Locate and identify every blood parasite.
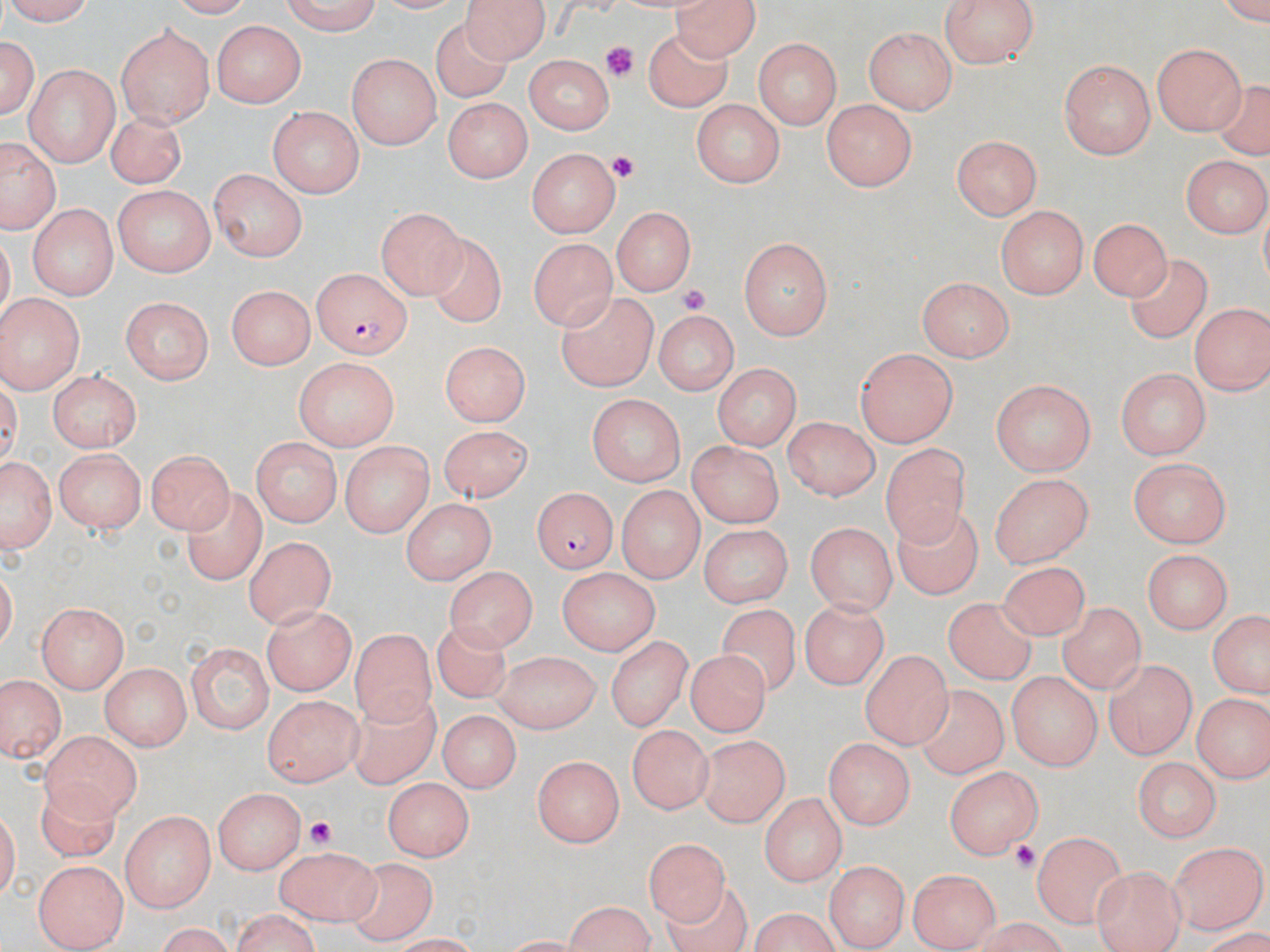
Approximate bounding boxes as (x1, y1, x2, y2) in pixels.
Plasmodium falciparum-infected red blood cells: (312, 266, 411, 358), (530, 488, 617, 574).
No Plasmodium ovale, Plasmodium malariae, Plasmodium vivax, Babesia divergens, or Trypanosoma brucei observed.

Uninfected red blood cell locations: (1, 0, 103, 26), (273, 0, 380, 35), (462, 0, 552, 62), (670, 0, 763, 57), (941, 1, 1041, 68), (429, 19, 511, 102), (209, 20, 310, 106), (114, 24, 213, 126), (865, 27, 956, 113), (645, 30, 734, 113), (0, 31, 38, 119), (751, 37, 844, 128), (1152, 39, 1247, 135), (348, 54, 439, 151), (524, 56, 615, 133), (1060, 60, 1157, 159), (23, 63, 118, 165), (1210, 81, 1270, 154), (445, 96, 529, 184), (689, 99, 787, 186), (821, 99, 919, 192), (268, 105, 366, 198), (101, 112, 188, 186), (951, 134, 1044, 223), (0, 135, 60, 236), (527, 146, 622, 237), (1180, 154, 1269, 238), (209, 169, 305, 262), (111, 186, 213, 276), (27, 202, 115, 301), (613, 204, 696, 293), (996, 205, 1090, 297), (376, 207, 463, 297), (1091, 214, 1172, 299), (430, 234, 510, 331), (526, 236, 620, 328), (739, 236, 834, 342), (1126, 257, 1213, 343), (918, 276, 1014, 360), (227, 284, 316, 370), (557, 292, 656, 390), (0, 294, 84, 395), (120, 297, 212, 385), (1188, 301, 1270, 394), (654, 310, 739, 394), (440, 342, 530, 429), (856, 349, 958, 447), (294, 356, 401, 452), (713, 364, 798, 452), (47, 367, 145, 452), (1114, 368, 1212, 457), (992, 381, 1096, 476), (585, 393, 686, 487), (779, 417, 883, 498), (435, 425, 535, 500), (250, 437, 338, 526), (341, 441, 431, 539), (687, 442, 782, 526), (880, 442, 970, 546), (54, 447, 144, 533), (147, 448, 233, 533), (0, 451, 55, 557), (1129, 454, 1229, 546), (990, 472, 1091, 569), (616, 484, 703, 583), (183, 485, 264, 590), (398, 498, 498, 582), (891, 508, 984, 597), (806, 519, 897, 612), (696, 523, 791, 607), (243, 536, 335, 628), (1142, 551, 1230, 635), (995, 562, 1097, 644), (444, 565, 536, 657), (555, 569, 657, 654), (946, 594, 1042, 683), (801, 598, 888, 692), (37, 603, 129, 690), (261, 604, 358, 693), (721, 604, 803, 696), (1055, 604, 1153, 691), (1204, 611, 1270, 700), (431, 619, 511, 702), (352, 627, 434, 723), (604, 631, 690, 729), (185, 642, 272, 733), (492, 649, 598, 732), (683, 649, 769, 737), (858, 649, 952, 745), (1106, 661, 1195, 760), (101, 666, 189, 749), (1006, 671, 1101, 772), (0, 679, 66, 765), (344, 686, 437, 797), (911, 686, 1004, 780), (1192, 692, 1267, 785), (263, 695, 362, 789), (436, 710, 520, 794), (625, 726, 713, 816), (693, 730, 787, 832), (41, 731, 141, 818), (823, 740, 914, 830), (533, 754, 622, 851), (1130, 756, 1221, 840), (943, 765, 1042, 859), (386, 781, 472, 861), (212, 789, 302, 874), (761, 792, 846, 889), (121, 811, 213, 912), (1032, 831, 1124, 928), (637, 834, 724, 918), (1168, 841, 1266, 936), (270, 844, 381, 924), (343, 860, 435, 941), (33, 861, 128, 950), (821, 861, 905, 949), (1090, 865, 1184, 950), (906, 869, 1000, 950), (666, 878, 751, 952), (557, 904, 654, 952), (751, 907, 837, 952), (226, 911, 324, 952), (149, 924, 237, 951). Platelet locations: (607, 44, 634, 82), (608, 153, 637, 184), (677, 284, 709, 317), (298, 814, 334, 850), (1009, 839, 1043, 875). Slide-level diagnosis: Plasmodium falciparum. Image is 1270×952 pixels. 1000x magnification. Single field of view. May-Grünwald-Giemsa-stained preparation. Light microscopy. Thin blood smear.